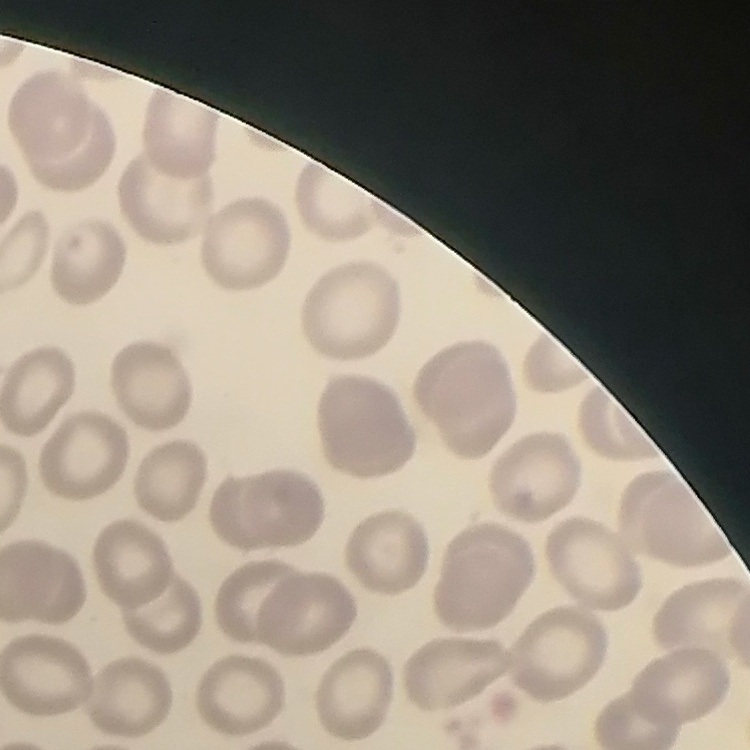

Summary:
  - Red blood cell morphology: no rouleaux formation
  - Image type: square crop of a larger photomicrograph
  - Stain: Field's or Giemsa
  - Preparation: thin blood smear